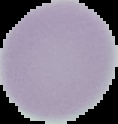 Image is 118×124 pixels. Result: no malaria parasites seen. Segmented cell region on a black background. From a thin blood smear.